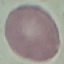
result: no malaria parasites detected
capture: smartphone through the microscope eyepiece
stain: Giemsa
image_type: cell patch, automatically extracted from a larger field of view and resized to 64 × 64 pixels
preparation: thin blood film